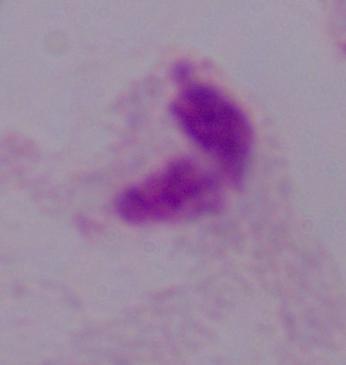
Summary:
  - Modality: photomicrograph
  - Identification: trichomonad
  - Magnification: 1000x